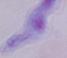
{
  "identification": "trypanosome",
  "magnification": "1000x",
  "modality": "photomicrograph"
}